Find the cells and give the type of each one.
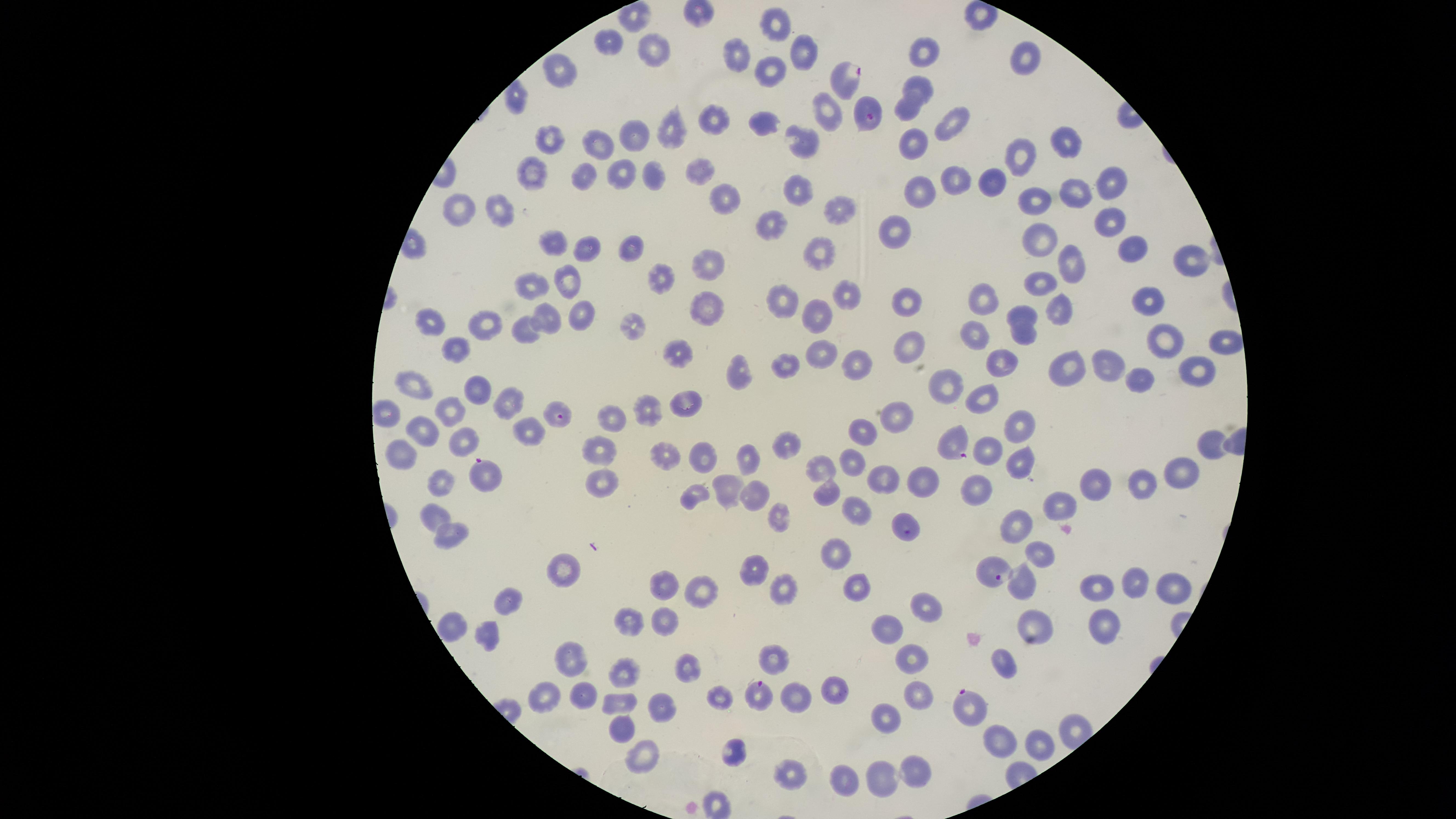

Approximate marker points as [x, y] in pixels.
Parasitized red blood cells: [846, 76], [867, 115], [557, 411], [950, 444], [487, 478], [989, 569], [760, 694], [966, 704].
Uninfected red blood cells: [781, 23], [605, 46], [928, 50], [800, 52], [737, 53], [657, 55], [1031, 56], [559, 71], [769, 74], [920, 87], [518, 99], [904, 110], [827, 112], [715, 117], [766, 122], [953, 123], [665, 132], [633, 133], [547, 135], [805, 139], [601, 142], [1063, 142], [911, 145], [1019, 161], [701, 170], [622, 173], [532, 174], [585, 174], [651, 175], [992, 180], [952, 181], [1110, 181], [794, 188], [918, 192], [725, 193], [1075, 194], [1035, 204], [464, 209], [839, 209], [500, 210], [1109, 221], [771, 222], [896, 233], [1041, 235], [553, 242], [587, 244], [1133, 244], [629, 247], [816, 255], [1188, 258], [1075, 260], [708, 267], [567, 275], [657, 278], [1045, 282], [536, 285], [848, 293], [909, 299], [980, 299], [1150, 302], [784, 303], [705, 308], [548, 312], [580, 312], [1059, 313], [818, 315], [1021, 317], [480, 322], [430, 324], [628, 330], [526, 331], [976, 331], [1026, 336], [1165, 337], [1220, 341], [455, 347], [909, 347], [821, 353], [678, 355], [784, 359], [858, 362], [1000, 363], [1109, 367], [1198, 367], [1074, 368], [742, 372], [1141, 379], [948, 384], [414, 386], [473, 388], [987, 391], [510, 399], [686, 402], [450, 411], [649, 412], [893, 415], [612, 419], [422, 426], [1022, 426], [531, 430], [863, 433], [461, 436], [788, 442], [1206, 444], [400, 450], [706, 451], [672, 452], [989, 452], [599, 453], [754, 457], [852, 460], [1022, 465], [817, 468], [1180, 471], [882, 476], [923, 481], [1098, 481], [1144, 481], [439, 482], [603, 482], [731, 484], [979, 489], [823, 490], [693, 492], [752, 497], [1069, 503], [435, 509], [854, 512], [781, 516], [905, 516], [1015, 518], [454, 532], [1039, 552], [840, 554], [567, 566], [755, 567], [858, 580], [1136, 582], [662, 583], [781, 584], [1095, 584], [1026, 585], [1171, 589], [698, 593], [507, 597], [925, 605], [667, 620], [452, 622], [631, 622], [1034, 625], [1104, 625], [489, 631], [890, 631], [774, 653], [914, 654], [572, 661], [1002, 661], [686, 664], [625, 673], [833, 682], [586, 692], [921, 692], [790, 693], [721, 694], [547, 696], [622, 700], [662, 705], [888, 714], [621, 728], [1002, 738], [1040, 742], [736, 751], [644, 755], [788, 762], [918, 769], [883, 773], [845, 778].
No white blood cells identified.

Summary:
  - Image size: 1456×819 pixels
  - Species: Plasmodium falciparum
  - Preparation: thin blood smear
  - Visible region: circular
  - Capture: smartphone photograph through the microscope eyepiece
  - Stain: Giemsa
  - Field of view: single